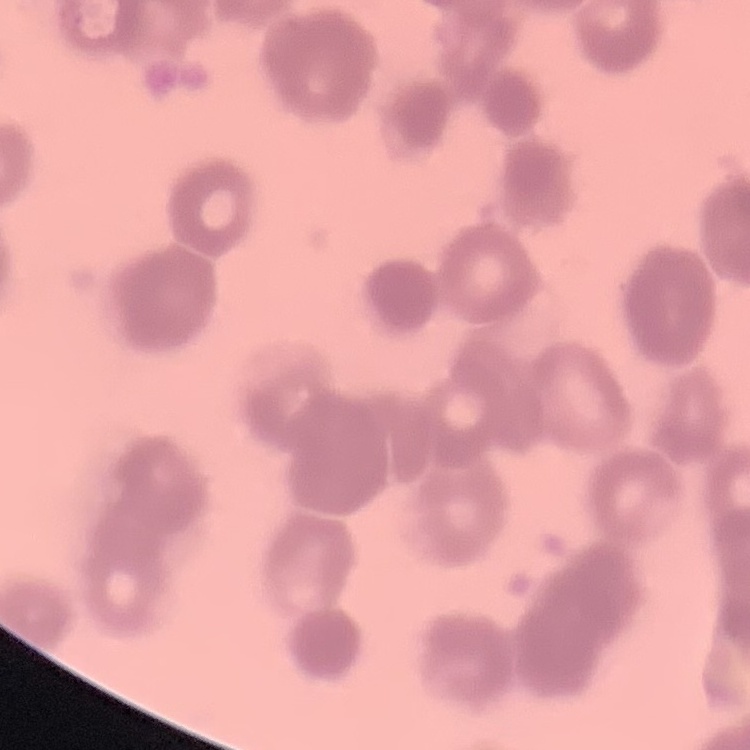

The red blood cells exhibit rouleaux formation. Thin blood smear. One tile cut from a larger photomicrograph. Field's or Giemsa stain.